Name the cell type shown.
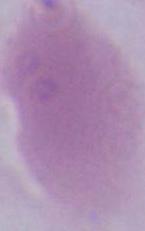

An erythrocyte.

magnification = 1000x
modality = photomicrograph